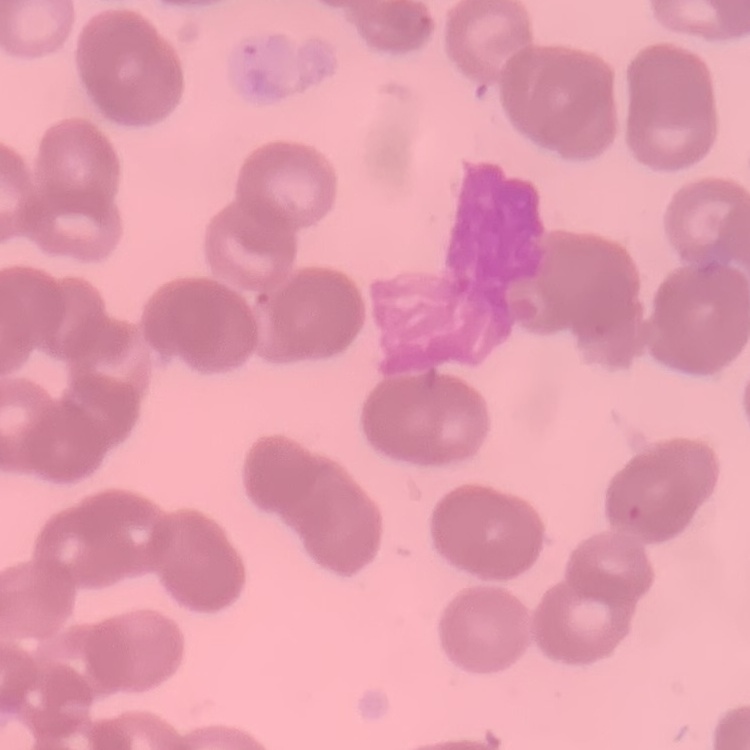
The red blood cells show rouleaux formation. Thin blood smear. Square crop of a larger photomicrograph. Field's or Giemsa stain.